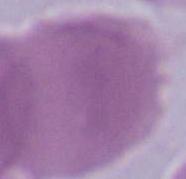
Summary:
  - Modality: micrograph
  - Magnification: 1000x
  - Identification: erythrocyte